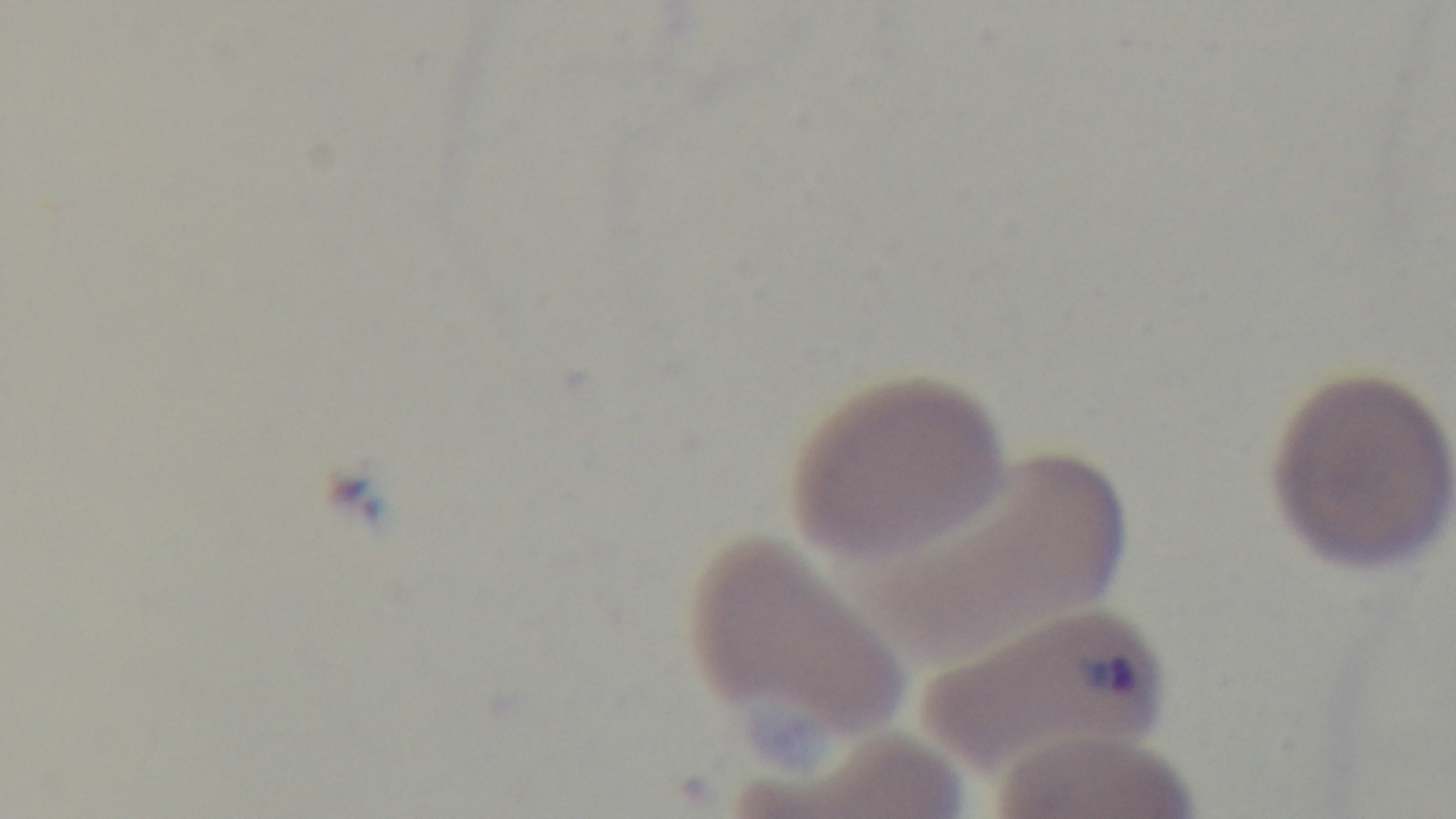

Summary:
  - Objective: 100x oil immersion
  - Capture: mounted 4K digital camera
  - Malaria status: positive
  - Preparation: thin blood film
  - Field of view: one from the slide
  - Stain: Giemsa
  - Modality: light microscopy